Identify the cell.
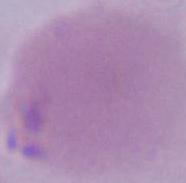

An erythrocyte.

{
  "modality": "photomicrograph",
  "magnification": "1000x"
}